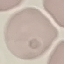

result: no malaria parasites seen
preparation: thin smear
image_type: cell patch, automatically extracted from a larger field of view and resized to 64 × 64 pixels
capture: smartphone through the microscope eyepiece
stain: Giemsa